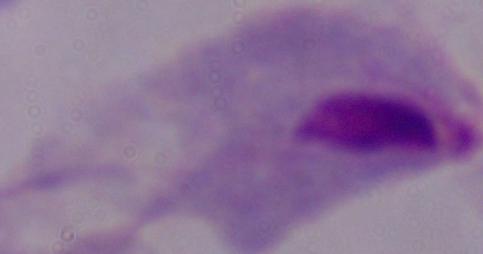
identification = trichomonad
modality = micrograph
magnification = 1000x